Comment on the morphology of the red blood cells.
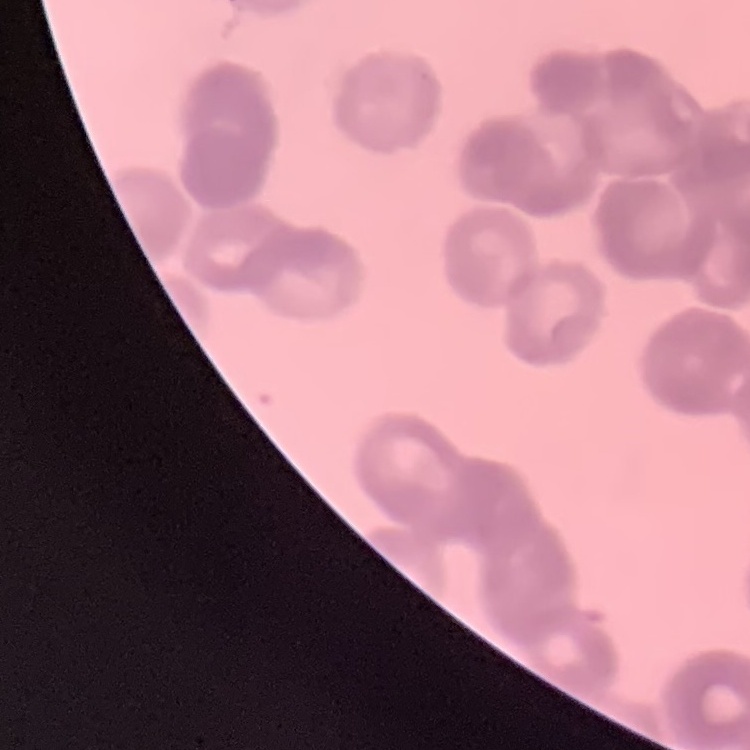

They show rouleaux formation.

Summary:
  - Image type: square crop of a larger photomicrograph
  - Stain: Field's or Giemsa
  - Preparation: thin blood film